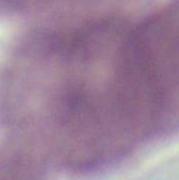

Summary:
  - Modality: photomicrograph
  - Identification: red blood cell
  - Magnification: 1000x